Locate every blood parasite and identify its species.
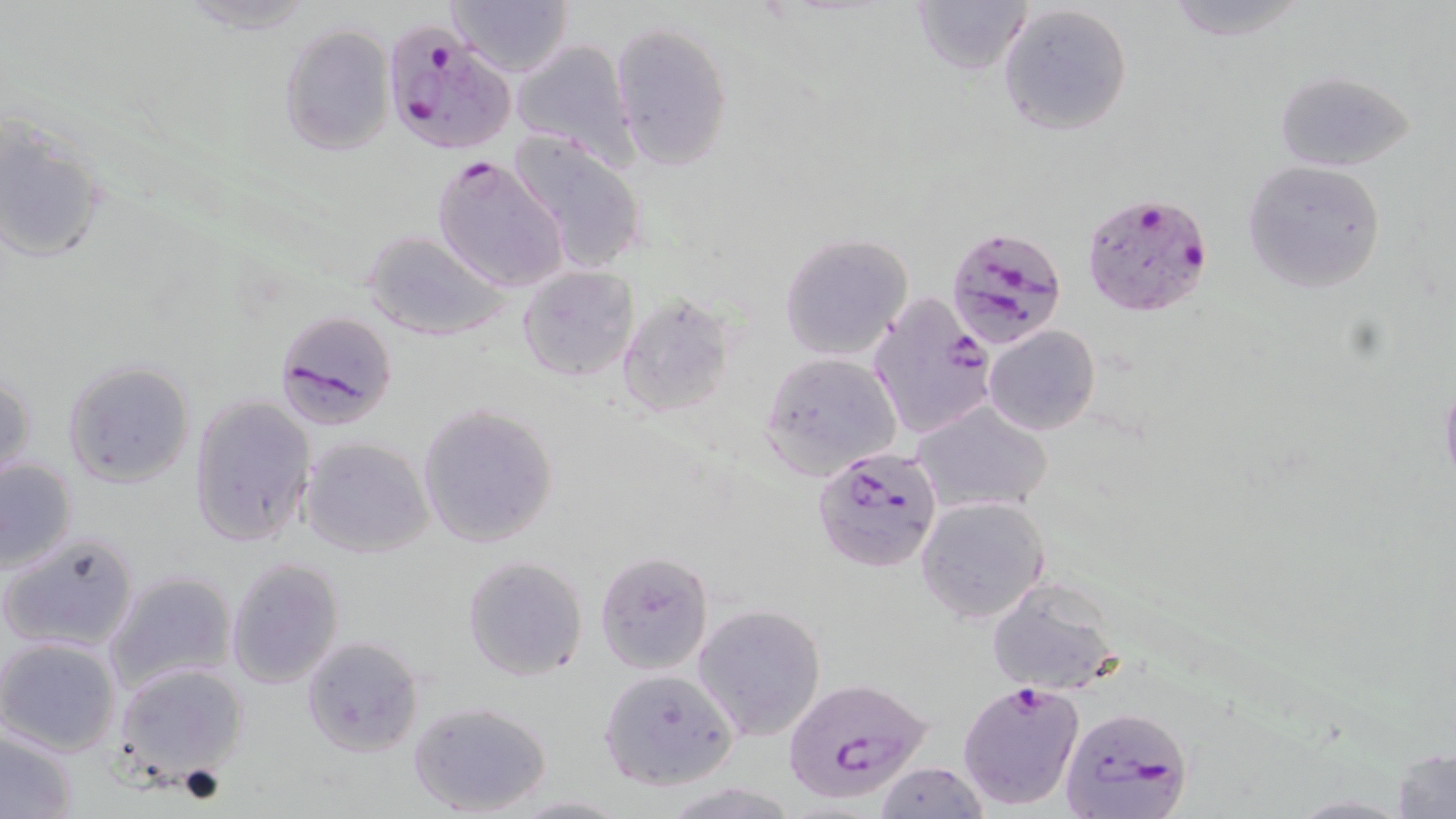

Approximate bounding boxes as named x1/y1/x2/y2 corners in pixels.
Plasmodium falciparum-infected red blood cells: (x1=381, y1=22, x2=514, y2=156), (x1=429, y1=154, x2=570, y2=293), (x1=1081, y1=193, x2=1213, y2=318), (x1=946, y1=225, x2=1069, y2=353), (x1=869, y1=291, x2=997, y2=439), (x1=275, y1=309, x2=398, y2=429), (x1=811, y1=445, x2=944, y2=574), (x1=785, y1=678, x2=936, y2=805), (x1=957, y1=679, x2=1085, y2=811), (x1=1057, y1=705, x2=1193, y2=819).
No Plasmodium ovale, Plasmodium malariae, Plasmodium vivax, Babesia divergens, or Trypanosoma brucei observed.

Summary:
  - Uninfected red blood cell locations: (x1=445, y1=0, x2=573, y2=77), (x1=1160, y1=0, x2=1311, y2=41), (x1=908, y1=1, x2=1031, y2=76), (x1=173, y1=2, x2=318, y2=33), (x1=996, y1=2, x2=1134, y2=135), (x1=610, y1=21, x2=733, y2=171), (x1=279, y1=24, x2=394, y2=156), (x1=509, y1=37, x2=637, y2=167), (x1=1275, y1=70, x2=1414, y2=171), (x1=1, y1=112, x2=107, y2=265), (x1=505, y1=129, x2=651, y2=273), (x1=1242, y1=160, x2=1387, y2=294), (x1=363, y1=230, x2=513, y2=342), (x1=778, y1=232, x2=915, y2=360), (x1=516, y1=264, x2=640, y2=384), (x1=617, y1=292, x2=736, y2=419), (x1=983, y1=325, x2=1102, y2=437), (x1=758, y1=351, x2=901, y2=478), (x1=62, y1=359, x2=195, y2=489), (x1=0, y1=371, x2=36, y2=490), (x1=1438, y1=374, x2=1456, y2=492), (x1=187, y1=394, x2=315, y2=549), (x1=911, y1=399, x2=1054, y2=516), (x1=417, y1=403, x2=559, y2=547), (x1=299, y1=435, x2=434, y2=558), (x1=0, y1=455, x2=78, y2=574), (x1=916, y1=494, x2=1049, y2=625), (x1=3, y1=530, x2=141, y2=652), (x1=594, y1=550, x2=715, y2=675), (x1=462, y1=554, x2=588, y2=680), (x1=225, y1=555, x2=345, y2=690), (x1=104, y1=570, x2=237, y2=692), (x1=987, y1=577, x2=1124, y2=696), (x1=692, y1=603, x2=826, y2=741), (x1=299, y1=633, x2=425, y2=758), (x1=0, y1=636, x2=122, y2=757), (x1=111, y1=663, x2=249, y2=783), (x1=598, y1=668, x2=739, y2=789), (x1=407, y1=701, x2=556, y2=818), (x1=0, y1=729, x2=77, y2=818), (x1=1390, y1=742, x2=1455, y2=818), (x1=872, y1=761, x2=988, y2=818), (x1=508, y1=794, x2=632, y2=817)
  - Slide-level diagnosis: Plasmodium falciparum
  - Field of view: one of a larger specimen
  - Image size: 1456×819 pixels
  - Magnification: 1000x
  - Preparation: thin blood film
  - Modality: light microscopy
  - Stain: May-Grünwald-Giemsa